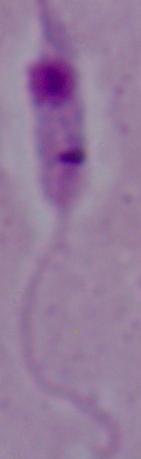

magnification = 1000x
identification = Leishmania
modality = photomicrograph